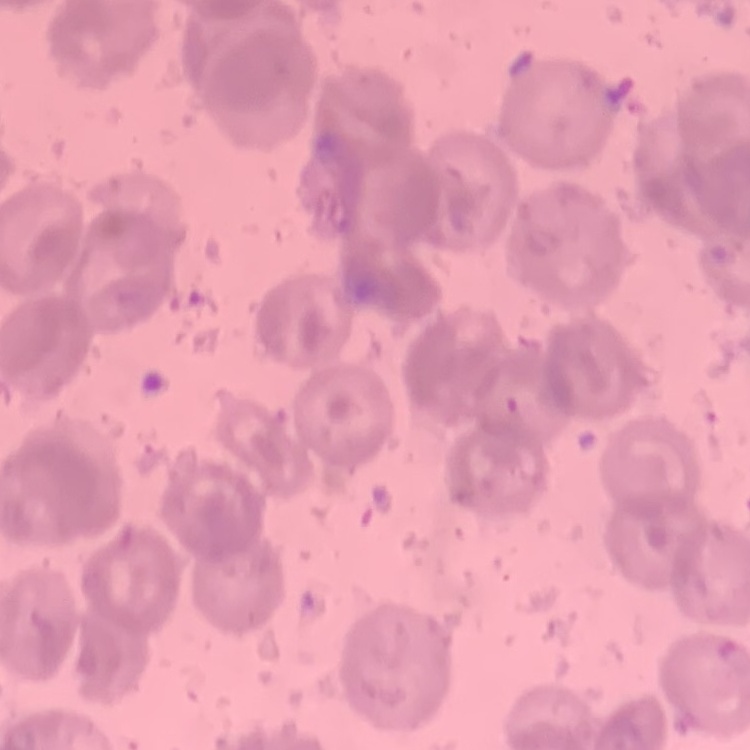

red blood cell morphology = no rouleaux formation
preparation = thin peripheral smear
stain = Field's or Giemsa
image type = one tile cut from a larger photomicrograph